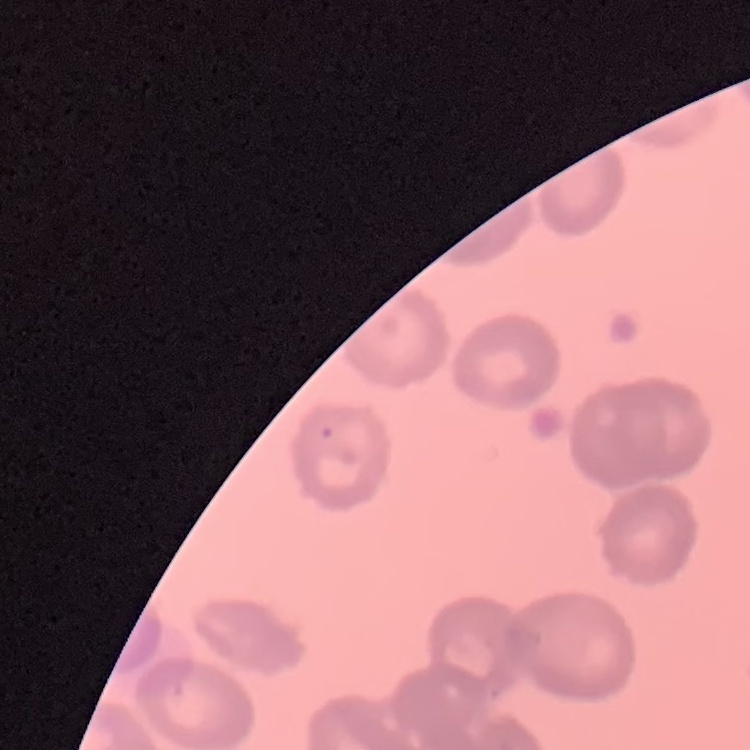
erythrocyte morphology = rouleaux formation
preparation = thin blood film
image type = one tile cut from a larger photomicrograph
stain = Field's or Giemsa